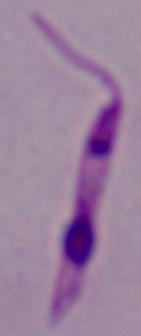

Summary:
  - Modality: micrograph
  - Magnification: 1000x
  - Identification: Leishmania